Locate every Plasmodium parasite.
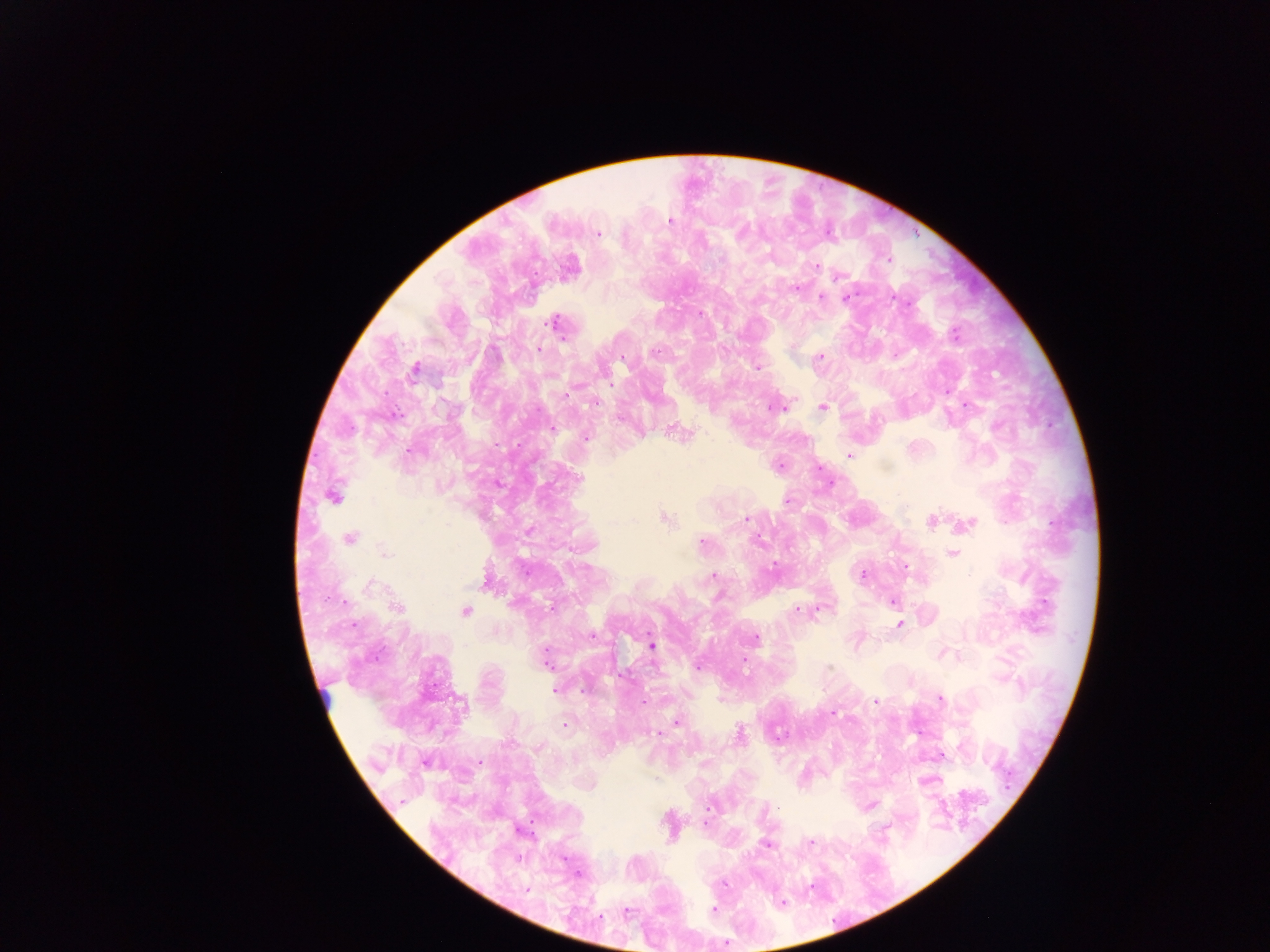

Approximate centers as x y in pixels.
Plasmodium parasites: 669 220; 743 232; 598 234; 701 243; 888 259; 817 266; 838 277; 798 287; 847 297; 822 298; 907 305; 703 314; 555 322; 955 336; 819 356; 755 367; 414 372; 566 394; 595 402; 775 407; 824 407; 553 427; 586 438; 520 445; 849 455; 333 497; 788 501; 746 517; 350 538; 758 541; 701 544; 384 554; 772 567; 715 575; 866 578; 368 583; 716 596; 326 598; 893 601; 345 603; 548 605; 796 608; 901 623; 354 624; 591 634; 754 638; 652 645; 545 649; 697 667; 830 669; 555 688; 940 700; 644 702; 876 702; 834 712; 564 725; 740 732; 781 735; 544 747; 708 807; 779 808; 766 843; 528 892; 783 901; 715 909; 726 944.

{
  "image_size": "1270×952 pixels",
  "field_of_view": "single",
  "country": "Ghana",
  "capture": "mobile-phone photograph through a microscope",
  "preparation": "thick blood smear"
}